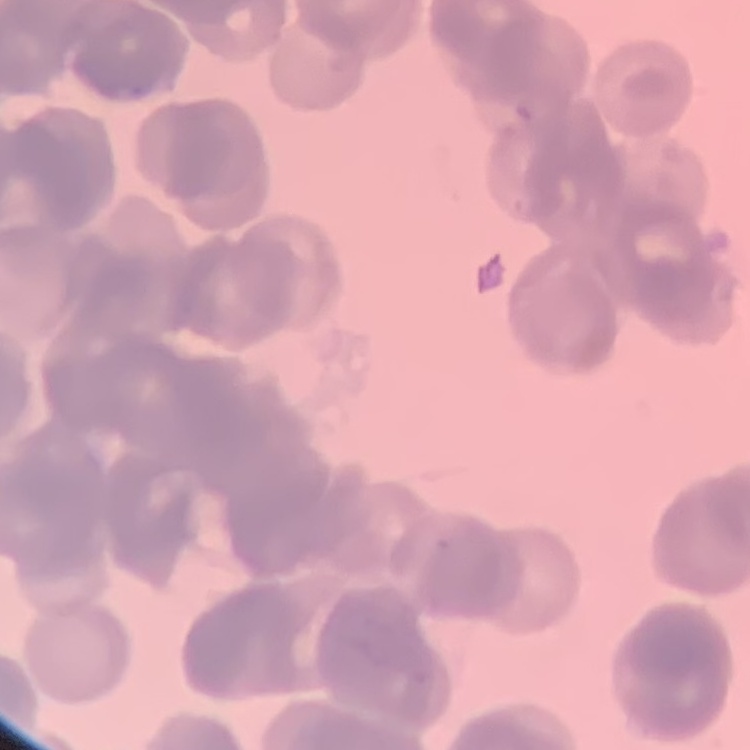

Summary:
  - Erythrocyte morphology: rouleaux formation
  - Stain: Field's or Giemsa
  - Image type: one tile cut from a larger photomicrograph
  - Preparation: thin blood smear